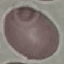
{
  "malaria_status": "uninfected",
  "stain": "Giemsa",
  "preparation": "thin smear",
  "image_type": "cell patch, automatically extracted from a larger field of view and resized to 64 × 64 pixels",
  "capture": "smartphone through the microscope eyepiece"
}